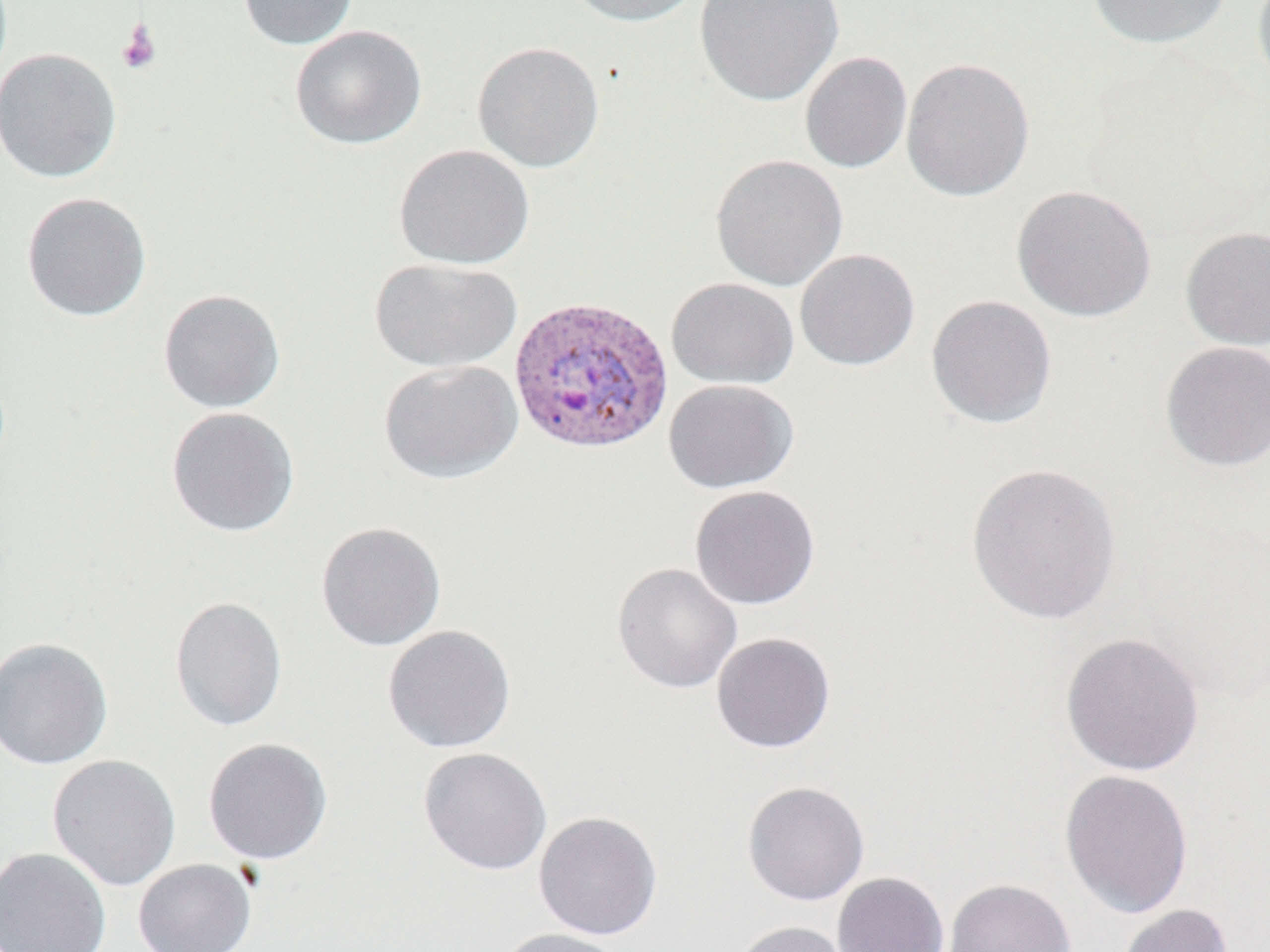

Summary:
  - Coordinate format: approximate bounding boxes as (x1,y1)-(x2,y2) corner pairs in pixels
  - Uninfected red blood cell locations: (237,0)-(359,50), (561,0)-(704,27), (695,0)-(843,107), (1087,0)-(1233,49), (1251,0)-(1270,97), (289,25)-(427,150), (472,41)-(605,172), (0,48)-(122,183), (799,51)-(912,174), (901,57)-(1035,202), (393,144)-(534,270), (710,154)-(849,291), (1011,184)-(1157,322), (21,192)-(152,321), (1180,226)-(1270,350), (795,248)-(920,371), (369,258)-(522,373), (666,277)-(799,389), (158,289)-(286,413), (926,295)-(1058,429), (1159,341)-(1270,472), (378,359)-(523,484), (663,379)-(799,493), (166,407)-(300,537), (965,461)-(1123,626), (689,485)-(821,610), (315,521)-(446,652), (612,562)-(743,694), (169,596)-(288,731), (382,624)-(516,753), (710,632)-(836,753), (1060,632)-(1205,776), (0,637)-(113,770), (203,737)-(333,864), (418,747)-(552,876), (46,753)-(181,891), (1059,769)-(1194,920), (741,780)-(870,906), (533,810)-(663,940), (0,846)-(112,952), (132,858)-(256,952), (832,871)-(949,952), (944,878)-(1077,952), (1117,903)-(1233,952), (730,920)-(854,952), (495,927)-(629,952)
  - Plasmodium vivax-infected red blood cell locations: (507,294)-(674,455)
  - Platelet locations: (117,19)-(161,76)
  - Slide-level diagnosis: Plasmodium vivax
  - Stain: May-Grünwald-Giemsa
  - Field of view: one of a larger specimen
  - Preparation: thin blood smear
  - Modality: light microscopy
  - Image size: 1270×952 pixels
  - Magnification: 1000x